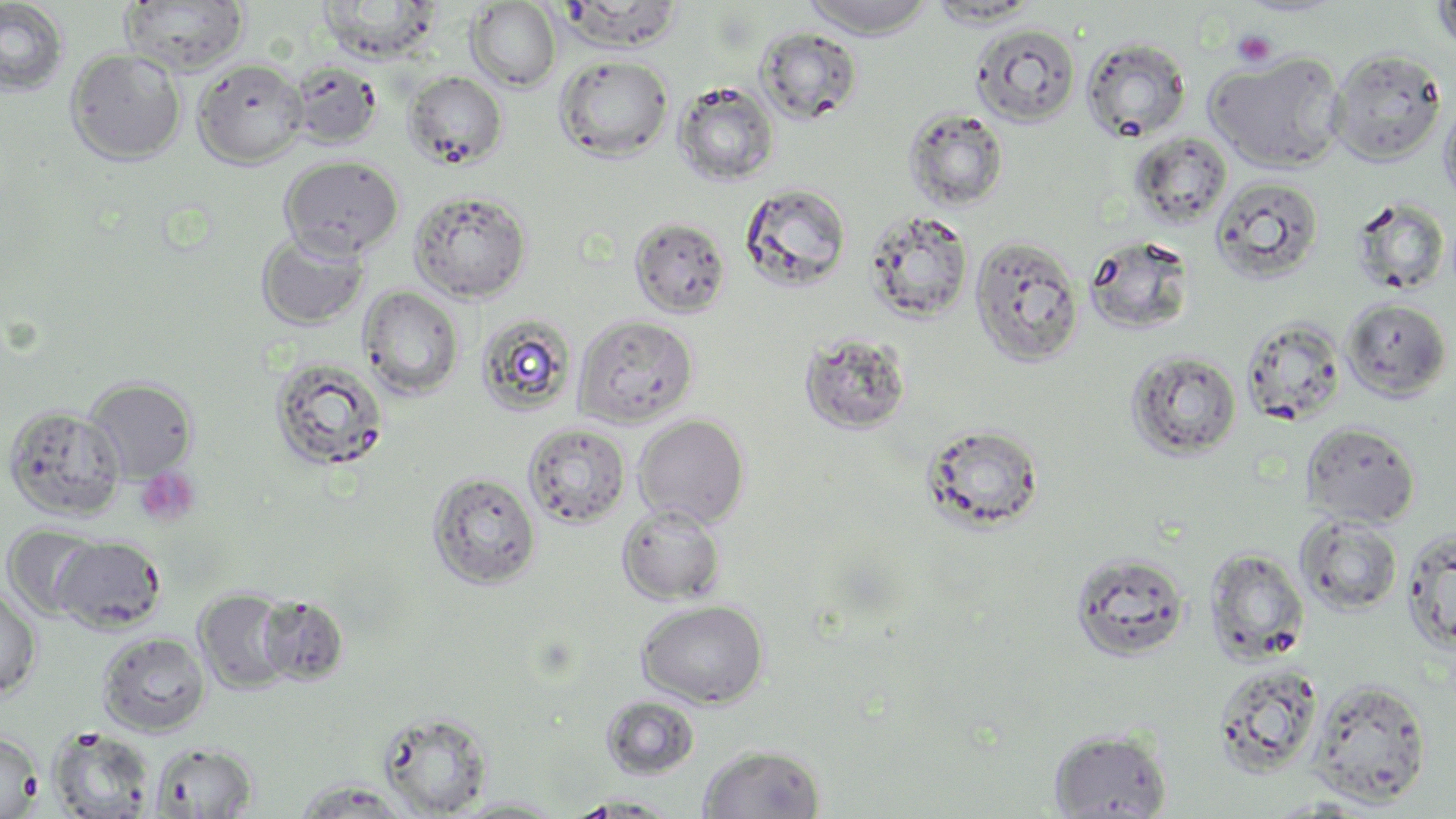 Approximate bounding boxes as (x1,y1)-(x2,y2) corner pairs in pixels. Uninfected red blood cell locations: (558,0)-(686,53), (803,0)-(936,38), (926,0)-(1042,27), (1430,0)-(1456,55), (0,1)-(70,97), (120,1)-(249,76), (317,1)-(443,64), (465,1)-(561,92), (970,23)-(1081,127), (757,27)-(863,125), (1080,37)-(1192,143), (64,47)-(186,165), (1328,47)-(1447,166), (1205,50)-(1346,173), (554,54)-(674,161), (193,57)-(309,168), (288,61)-(383,149), (403,71)-(508,170), (672,80)-(779,186), (1439,93)-(1456,213), (903,107)-(1010,211), (1128,132)-(1233,231), (279,156)-(404,259), (1210,175)-(1324,284), (739,182)-(852,293), (409,189)-(532,303), (1350,196)-(1452,297), (863,209)-(974,323), (628,216)-(731,319), (255,229)-(370,330), (969,235)-(1085,367), (1083,235)-(1196,335), (358,286)-(464,400), (1340,297)-(1453,401), (475,313)-(579,417), (573,315)-(699,428), (1241,315)-(1348,427), (799,330)-(913,435), (1125,349)-(1243,461), (269,356)-(390,473), (83,377)-(198,481), (2,404)-(126,522), (633,414)-(750,527), (1301,421)-(1421,527), (523,422)-(631,528), (920,422)-(1045,535), (426,471)-(542,589), (616,503)-(726,605), (1295,514)-(1403,617), (2,523)-(104,620), (1401,528)-(1456,655), (52,536)-(166,634), (1205,547)-(1311,665), (1070,551)-(1191,662), (0,586)-(42,700), (194,588)-(296,693), (257,594)-(349,686), (636,599)-(770,709), (97,632)-(211,736), (1212,662)-(1323,778), (1307,678)-(1432,806), (601,696)-(699,780), (377,711)-(493,816), (47,727)-(156,819), (1048,727)-(1174,818), (0,732)-(42,818), (149,741)-(257,817), (697,744)-(826,819), (290,779)-(419,819), (566,794)-(681,817), (447,797)-(568,817). Platelet locations: (1232,29)-(1277,69), (135,467)-(201,528). Slide-level diagnosis: negative for blood parasites. May-Grünwald-Giemsa-stained preparation. Single field of view. Thin blood film. Light microscopy. Captured at 1000x magnification. Image is 1456×819 pixels.